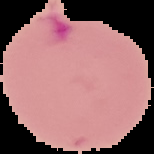

{
  "preparation": "thin blood film",
  "image_size": "154×154 pixels",
  "image_type": "cell region segmented out of the field of view; surrounding area masked to black",
  "result": "Plasmodium parasites detected"
}